State which parasite is depicted.
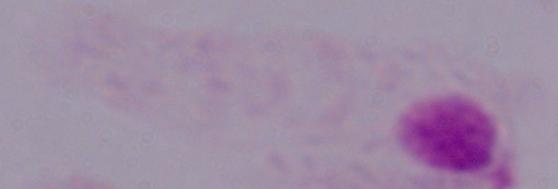

A trichomonad.

modality = micrograph
magnification = 1000x